Assess the morphology of the red blood cells.
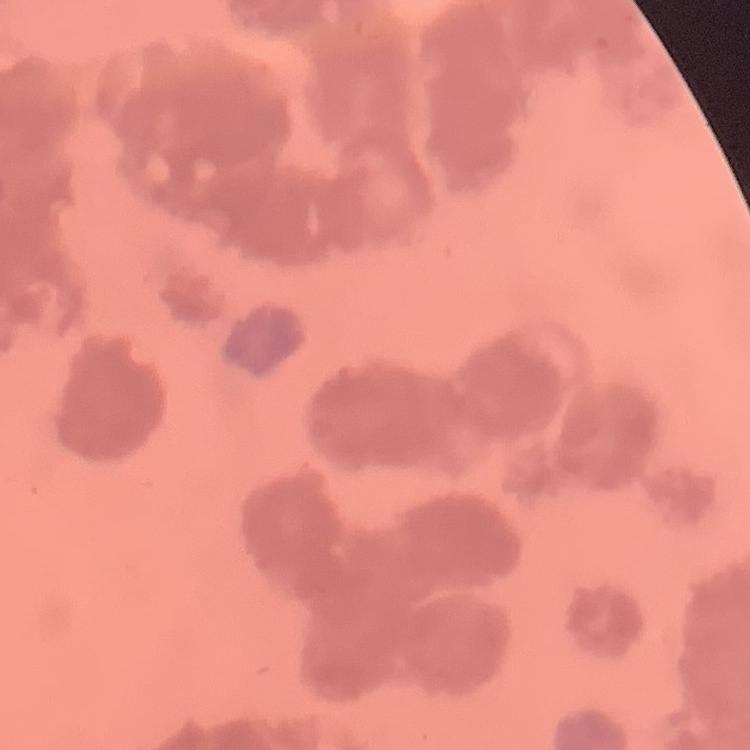
Rouleaux formation.

Summary:
  - Stain: Field's or Giemsa
  - Image type: square crop of a larger photomicrograph
  - Preparation: thin peripheral smear